Draw a bounding box around every artifact (platelet-like body, stain precipitate, or debris).
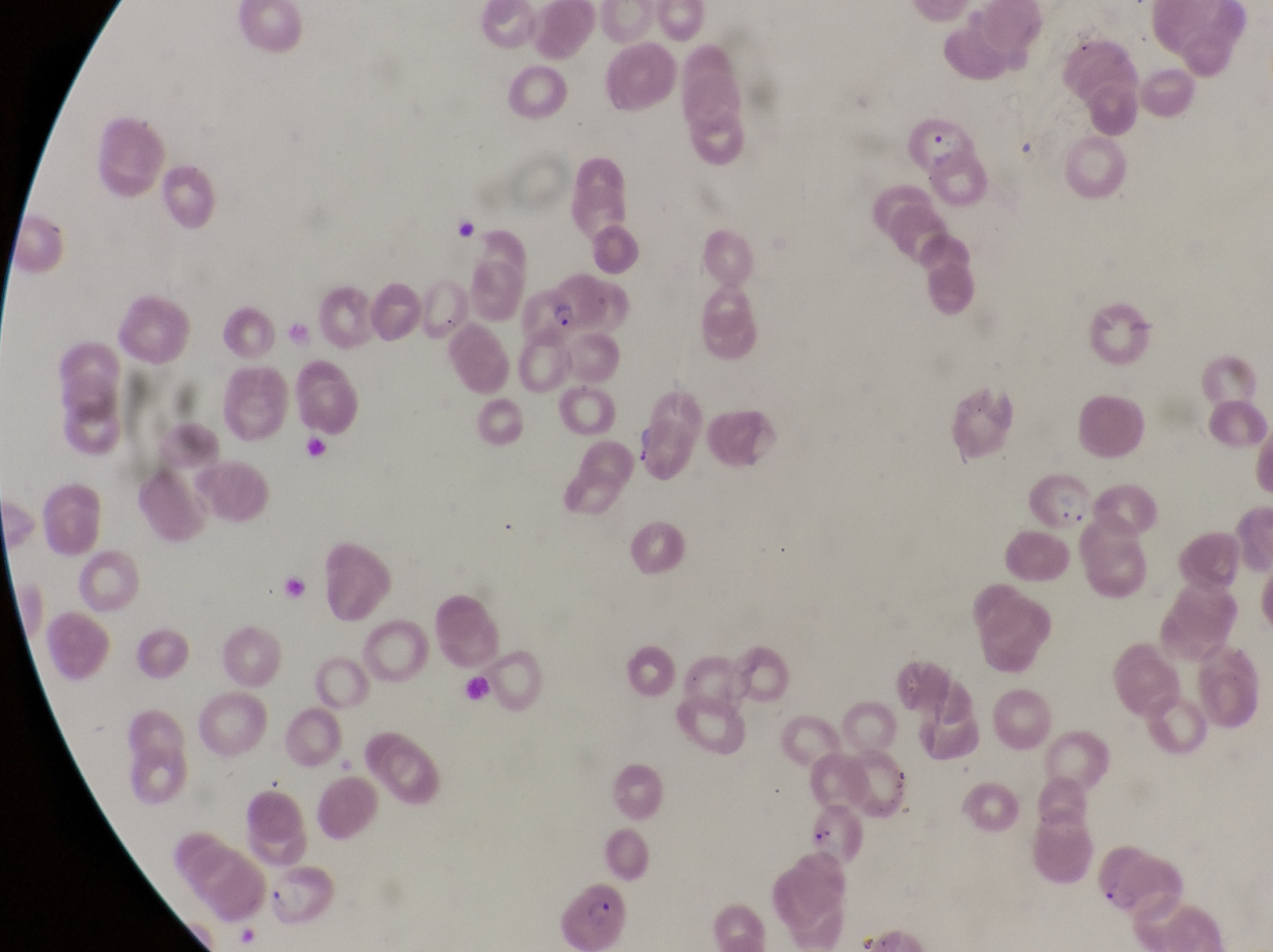
Approximate bounding boxes as left top right bottom in pixels.
Artifacts (platelet-like body, stain precipitate, or debris): 804 809 865 866; 270 871 343 927.

magnification = 1000x
capture = smartphone photograph through the eyepiece of an Olympus CX-23 microscope
parasitised red blood cell locations = approximate bounding boxes as left top right bottom in pixels: 908 107 970 168; 521 283 583 343; 1026 455 1096 529; 1095 847 1183 922; 551 874 631 951
image size = 1273×952 pixels
country = Uganda
preparation = thin blood film
field of view = single